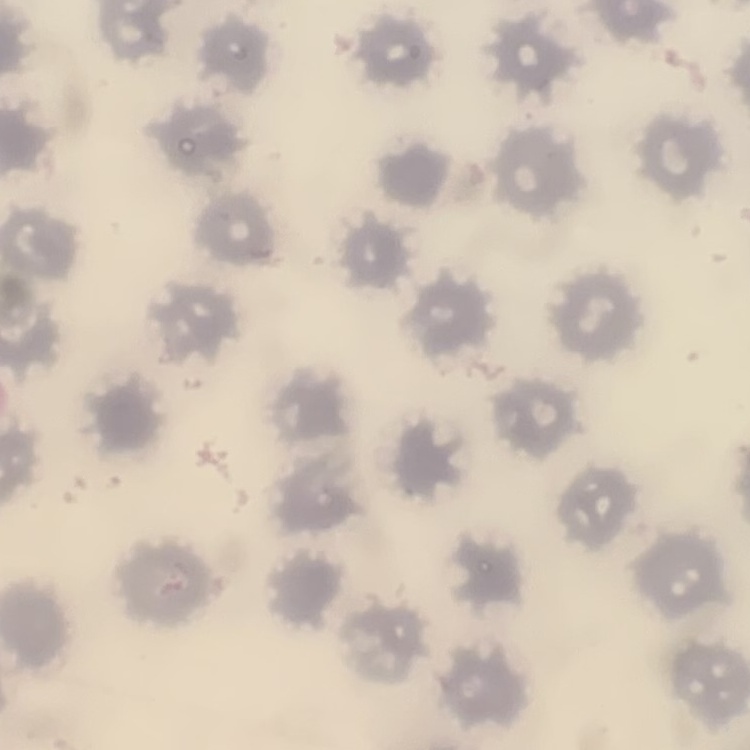

The erythrocytes exhibit no rouleaux formation. Thin blood film. One tile cut from a larger photomicrograph. Field's or Giemsa stain.